Report the malaria status of this cell.
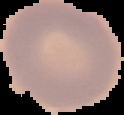
Uninfected.

image size = 124×115 pixels
preparation = thin blood smear
image type = cell region segmented out of the field of view; surrounding area masked to black